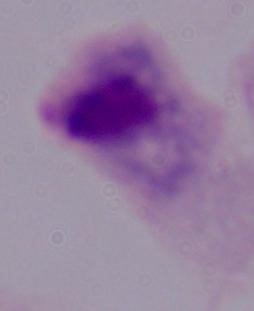
Summary:
  - Identification: trichomonad
  - Modality: photomicrograph
  - Magnification: 1000x